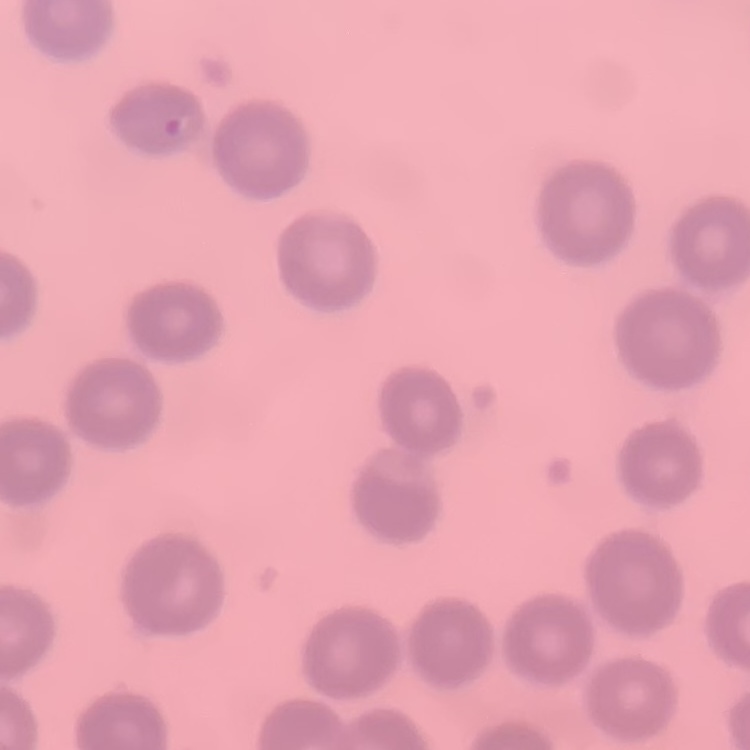

Summary:
  - Erythrocyte morphology: no rouleaux formation
  - Image type: one tile cut from a larger photomicrograph
  - Preparation: thin blood smear
  - Stain: Field's or Giemsa